Describe the morphology of the erythrocytes.
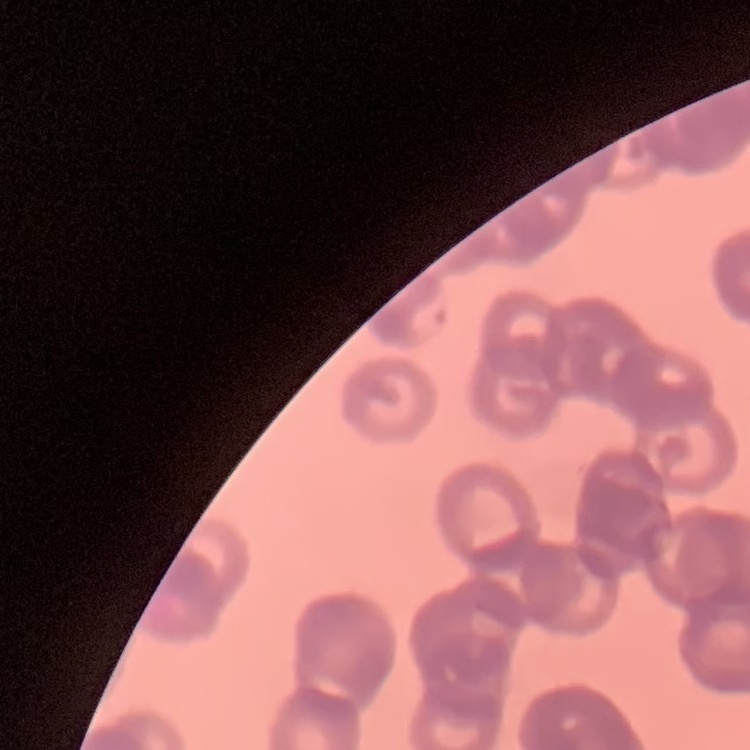

They show rouleaux formation.

preparation = thin peripheral smear
stain = Field's or Giemsa
image type = one tile cut from a larger photomicrograph